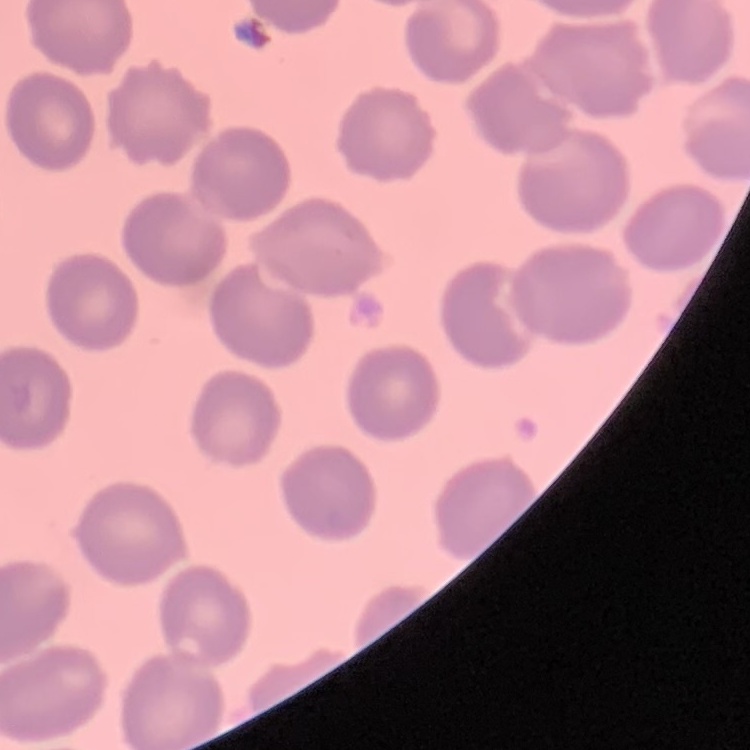

red_blood_cell_morphology: no rouleaux formation
preparation: thin peripheral smear
stain: Field's or Giemsa
image_type: one tile cut from a larger photomicrograph